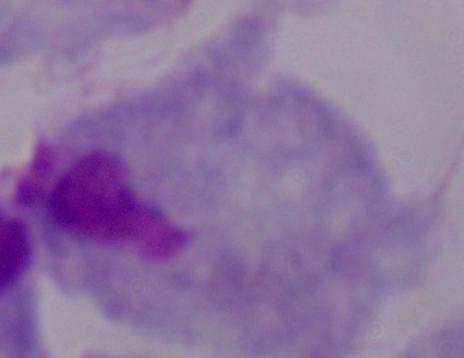
Summary:
  - Magnification: 1000x
  - Modality: photomicrograph
  - Identification: trichomonad